Locate every blood parasite and identify its species.
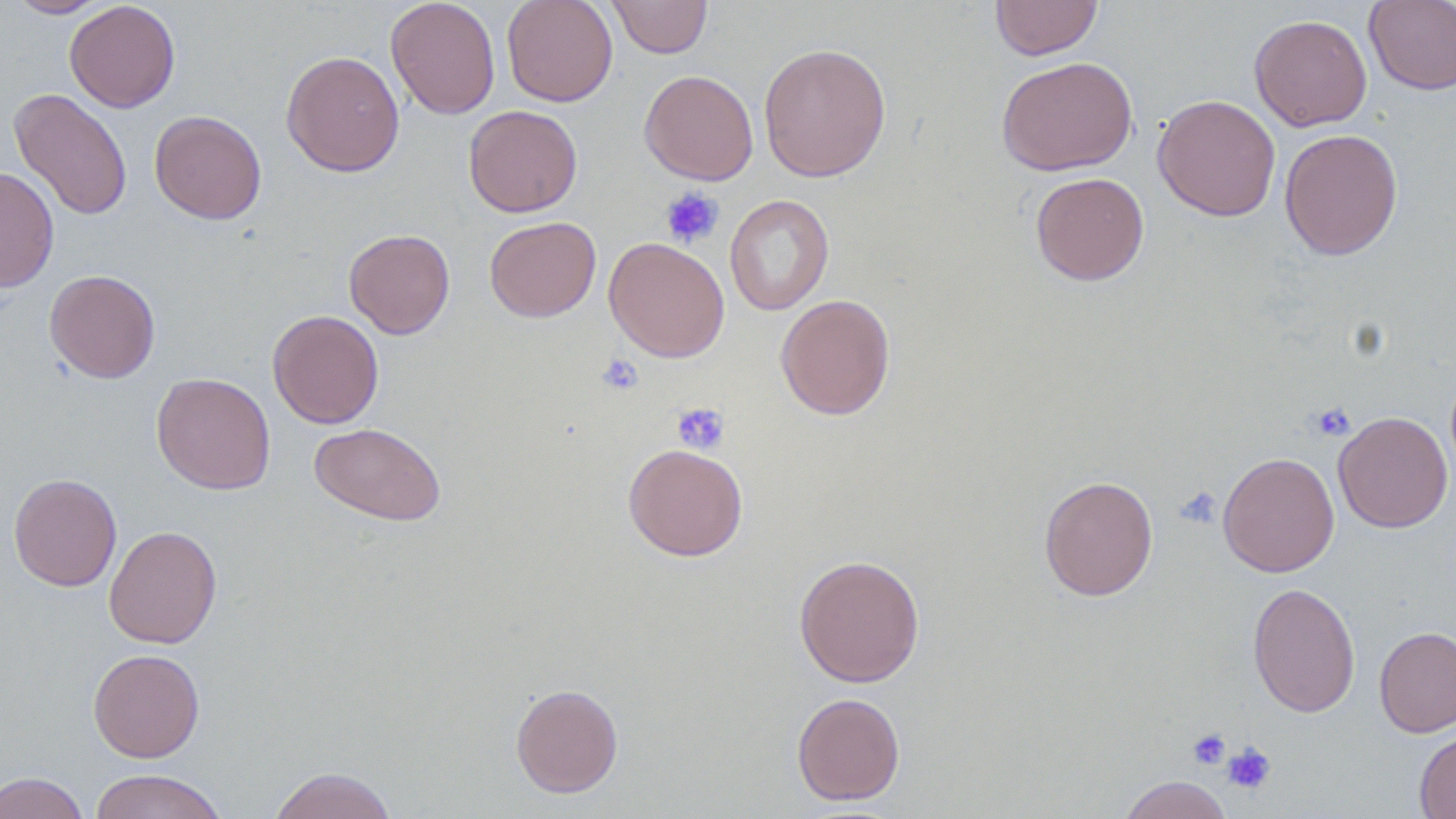

No blood parasites observed.

slide_level_diagnosis: negative for blood parasites
field_of_view: single
image_size: 1456×819 pixels
stain: May-Grünwald-Giemsa
platelet_locations: 'approximate bounding boxes as (x1, y1, x2, y2) in pixels: (660, 187, 724, 248), (596, 354, 644, 397), (672, 402, 730, 454), (1310, 403, 1356, 442), (1176, 486, 1223, 530), (1187, 728, 1231, 770), (1221, 742, 1276, 795)'
modality: optical microscopy
magnification: 1000x
uninfected_red_blood_cell_locations: 'approximate bounding boxes as (x1, y1, x2, y2) in pixels: (6, 0, 112, 18), (386, 0, 501, 119), (501, 0, 618, 107), (607, 0, 713, 58), (990, 0, 1103, 60), (1363, 0, 1456, 95), (64, 1, 180, 112), (1249, 13, 1372, 132), (758, 42, 891, 183), (281, 50, 405, 177), (996, 55, 1138, 176), (639, 69, 758, 185), (9, 88, 133, 221), (1152, 93, 1281, 221), (463, 104, 583, 217), (150, 110, 267, 225), (1279, 128, 1403, 260), (1, 167, 58, 293), (1030, 171, 1149, 286), (724, 194, 834, 316), (484, 216, 601, 322), (343, 228, 456, 339), (604, 236, 730, 363), (44, 269, 160, 383), (775, 294, 895, 420), (267, 309, 384, 429), (151, 373, 276, 495), (1333, 410, 1453, 533), (309, 422, 447, 526), (622, 443, 748, 561), (1218, 451, 1340, 577), (8, 473, 122, 591), (1038, 475, 1159, 601), (103, 525, 222, 649), (793, 553, 925, 688), (1247, 583, 1361, 717), (1374, 626, 1456, 737), (88, 648, 205, 762), (510, 682, 623, 798), (791, 692, 905, 805), (1414, 728, 1456, 819), (267, 766, 398, 819), (89, 769, 229, 819), (0, 771, 90, 819), (1117, 774, 1235, 819)'
preparation: thin blood film